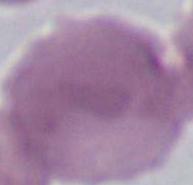

identification = erythrocyte
magnification = 1000x
modality = micrograph